Give the position of every Plasmodium parasite visible.
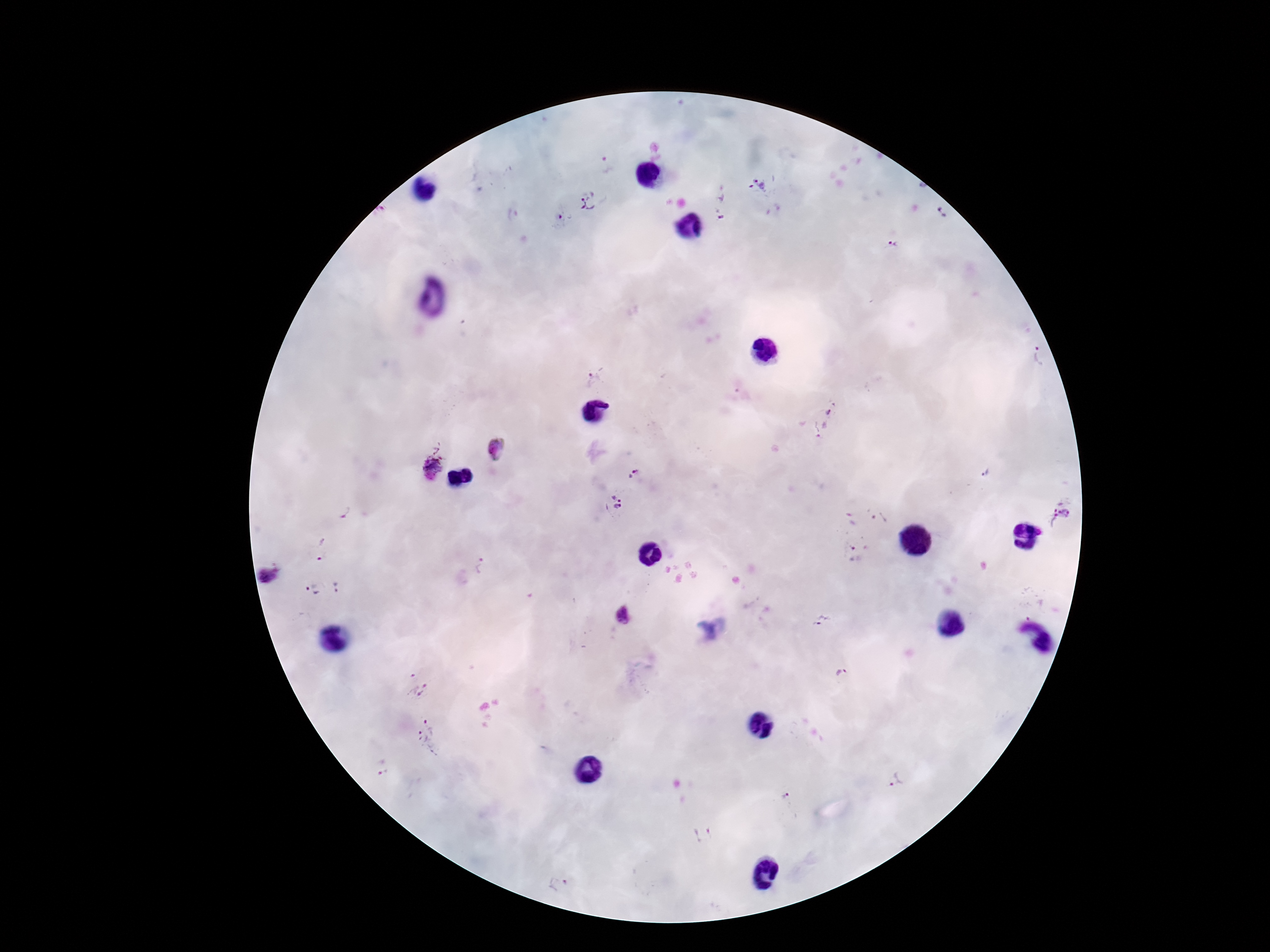
Approximate centers as [x, y] in pixels.
Plasmodium parasites: [604, 165], [759, 185], [590, 202], [718, 204], [941, 214], [564, 217], [892, 244], [1038, 355], [595, 379], [827, 421], [495, 450], [427, 465], [986, 471], [633, 474], [612, 504], [345, 513], [1061, 514], [868, 515], [320, 550], [856, 551], [481, 566], [269, 574], [311, 582], [337, 587], [624, 615], [824, 620], [842, 675], [416, 681], [429, 737], [382, 767], [895, 780], [784, 798], [703, 834], [559, 885].

Summary:
  - Capture: smartphone camera through the microscope eyepiece
  - Magnification: 100x
  - Field of view: one from this slide
  - Patient malaria status: infected
  - Stain: Giemsa
  - Preparation: thick blood film
  - Image size: 1270×952 pixels